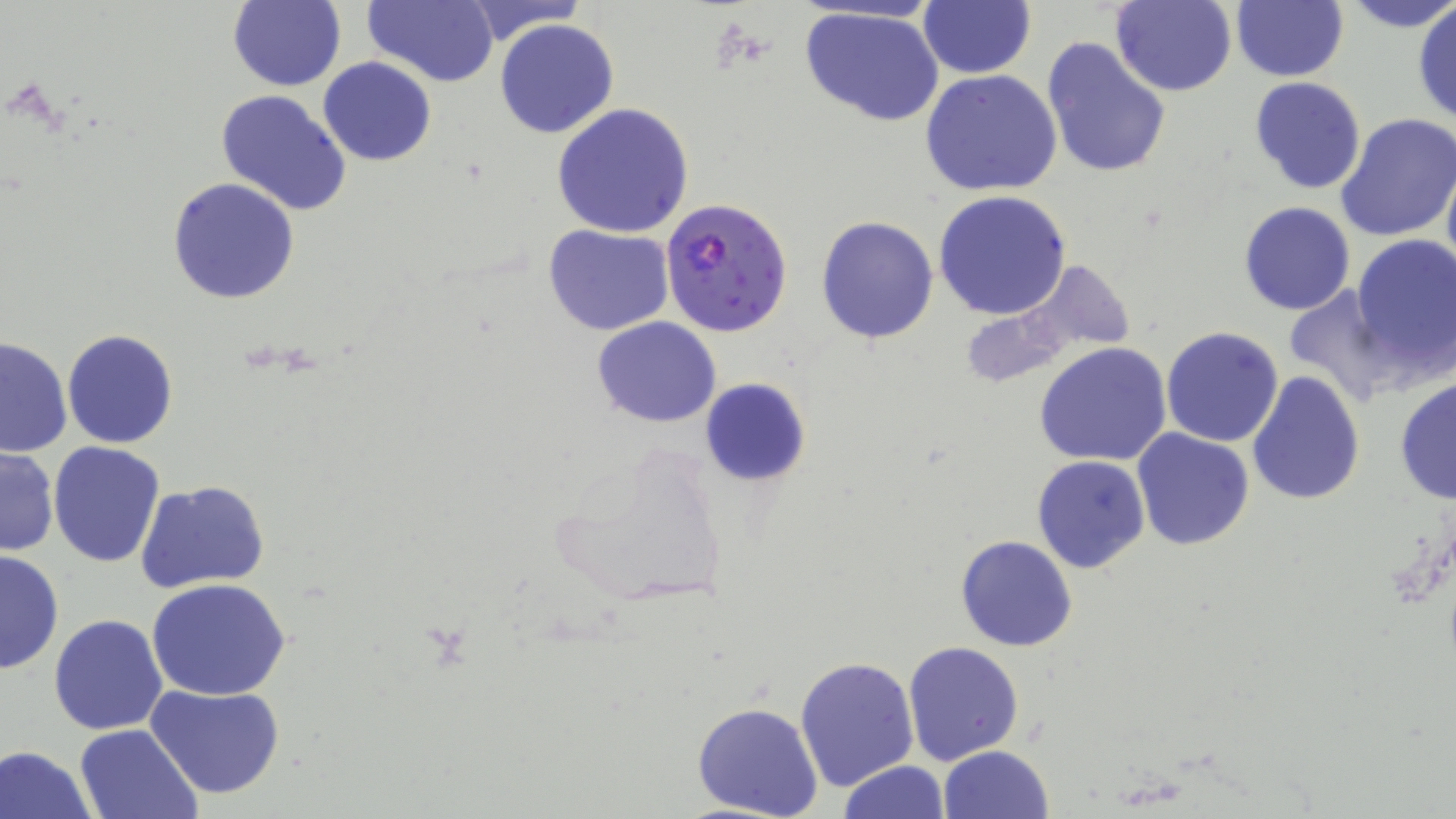

Summary:
  - Coordinate format: approximate bounding boxes as (x1, y1, x2, y2) in pixels
  - Uninfected red blood cell locations: (363, 0, 498, 87), (456, 0, 587, 45), (918, 0, 1036, 79), (1341, 0, 1456, 33), (227, 1, 345, 92), (1111, 1, 1238, 97), (1230, 2, 1348, 82), (1412, 2, 1456, 126), (799, 7, 946, 127), (494, 18, 619, 139), (1041, 36, 1171, 180), (319, 56, 436, 166), (920, 69, 1063, 196), (1248, 76, 1367, 196), (214, 88, 353, 216), (551, 103, 695, 238), (1336, 114, 1456, 243), (1442, 158, 1456, 281), (168, 177, 300, 303), (934, 190, 1075, 321), (1237, 200, 1358, 315), (816, 215, 940, 344), (542, 224, 674, 335), (1351, 233, 1456, 380), (1279, 282, 1398, 407), (592, 316, 722, 427), (1160, 326, 1286, 447), (62, 329, 178, 448), (0, 336, 74, 458), (1034, 342, 1173, 466), (1245, 370, 1365, 507), (1393, 375, 1455, 506), (699, 377, 812, 488), (1132, 429, 1255, 551), (544, 438, 734, 610), (48, 441, 165, 568), (1, 446, 59, 558), (1031, 455, 1151, 575), (137, 480, 269, 594), (954, 535, 1078, 653), (0, 550, 64, 675), (147, 579, 295, 701), (48, 614, 168, 736), (903, 640, 1024, 764), (795, 656, 921, 794), (146, 683, 287, 800), (691, 700, 824, 819), (75, 723, 202, 818), (1, 743, 98, 819), (938, 744, 1054, 819), (837, 760, 948, 819)
  - Plasmodium falciparum-infected red blood cell locations: (660, 199, 793, 338)
  - Slide-level diagnosis: Plasmodium falciparum
  - Modality: optical microscopy
  - Magnification: 1000x
  - Preparation: thin blood film
  - Stain: May-Grünwald-Giemsa
  - Field of view: single
  - Image size: 1456×819 pixels